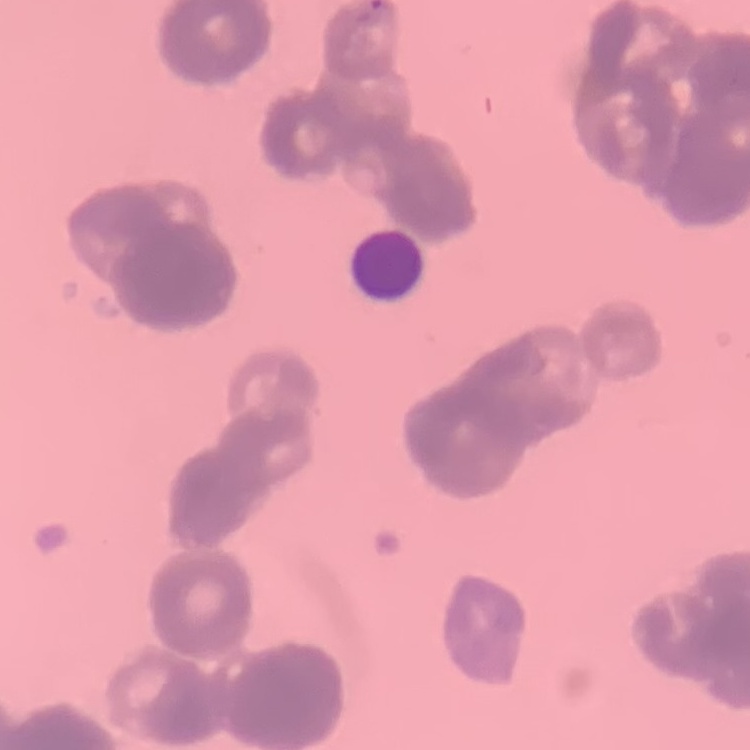
Summary:
  - Red blood cell morphology: rouleaux formation
  - Stain: Field's or Giemsa
  - Image type: one tile cut from a larger photomicrograph
  - Preparation: thin blood smear